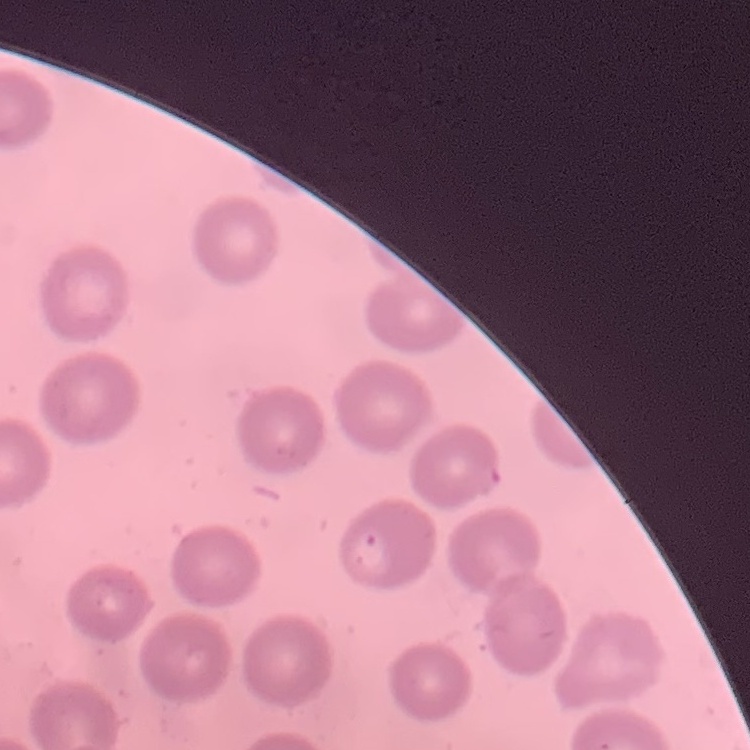

The erythrocytes exhibit no rouleaux formation. Stained with either Field's or Giemsa. Thin peripheral smear. Square crop of a larger photomicrograph.